Name the parasite shown.
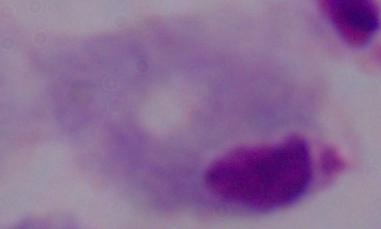

This is a trichomonad.

magnification = 1000x
modality = photomicrograph